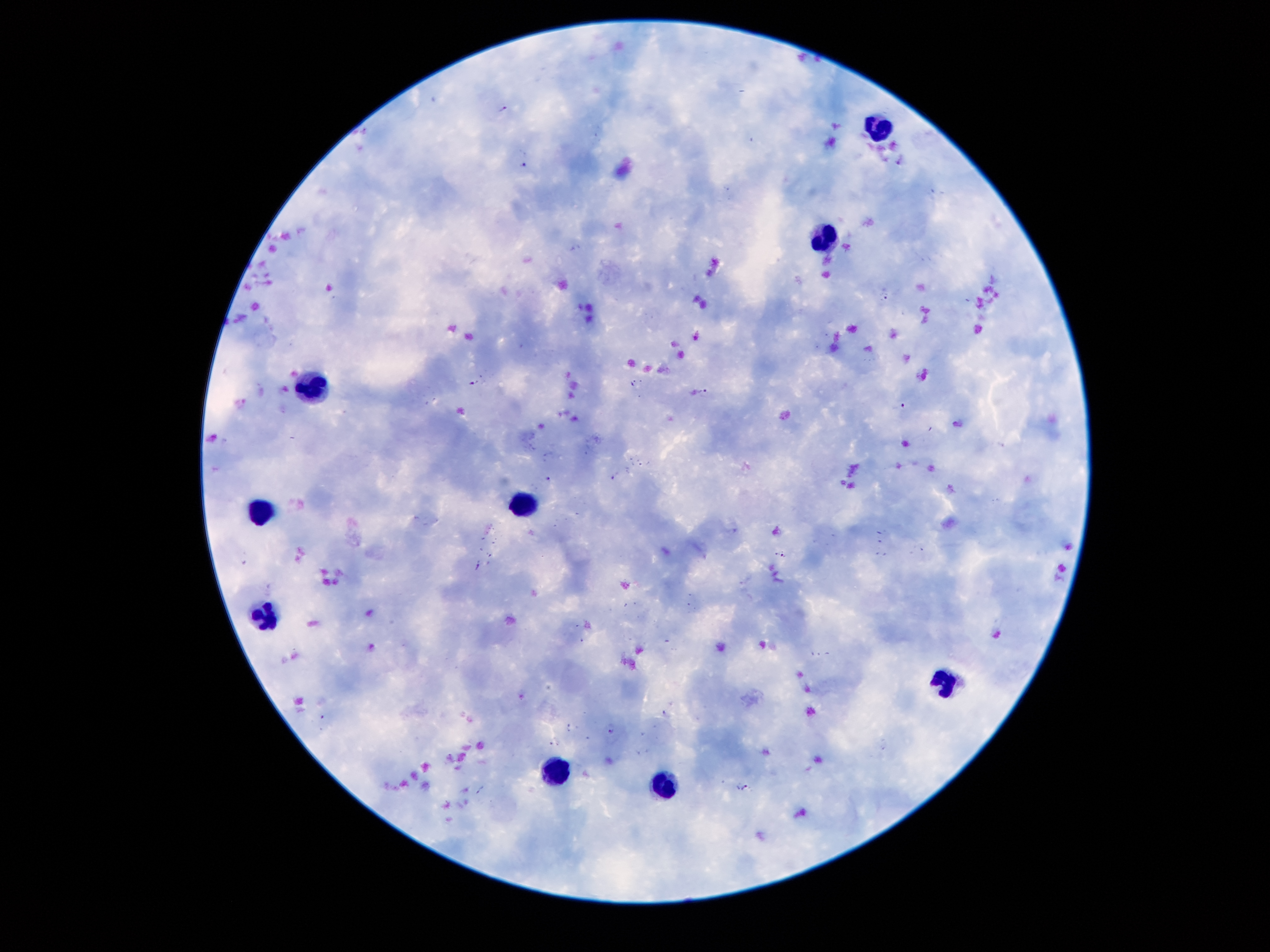
Approximate object centers, in pixels from the top-left corner.
Summary:
  - Plasmodium parasite locations: (x=503, y=107), (x=523, y=162), (x=886, y=298), (x=474, y=382), (x=704, y=390), (x=900, y=406), (x=549, y=477), (x=614, y=479), (x=781, y=555), (x=478, y=566), (x=665, y=712), (x=611, y=732), (x=745, y=788)
  - Leukocyte locations: (x=877, y=134), (x=828, y=241), (x=308, y=389), (x=522, y=502), (x=265, y=509), (x=264, y=616), (x=943, y=676), (x=552, y=771), (x=663, y=788)
  - Stain: Giemsa
  - Patient malaria status: infected with Plasmodium falciparum
  - Preparation: thick blood film
  - Magnification: 100x
  - Image size: 1270×952 pixels
  - Field of view: single
  - Capture: smartphone camera through the microscope eyepiece